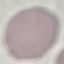
Summary:
  - Malaria status: uninfected
  - Capture: smartphone camera at the microscope eyepiece
  - Preparation: thin smear
  - Stain: Giemsa
  - Image type: automatically extracted cell patch, resized to 64 × 64 pixels